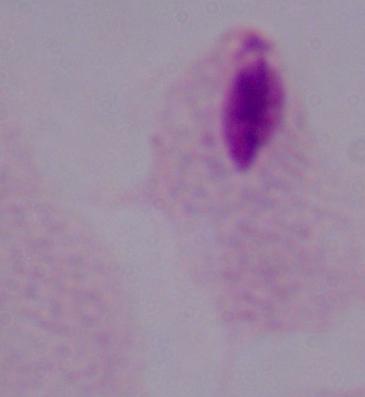 Captured at 1000x magnification. Micrograph. A trichomonad is seen.